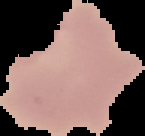

Summary:
  - Image type: cell region segmented out of the field of view; surrounding area masked to black
  - Result: negative for malaria parasites
  - Image size: 145×136 pixels
  - Preparation: thin blood smear